Classify this cell by malaria status.
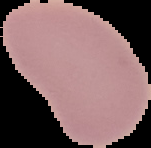
It is uninfected.

Summary:
  - Image size: 151×148 pixels
  - Preparation: thin blood film
  - Image type: segmented cell region on a black background